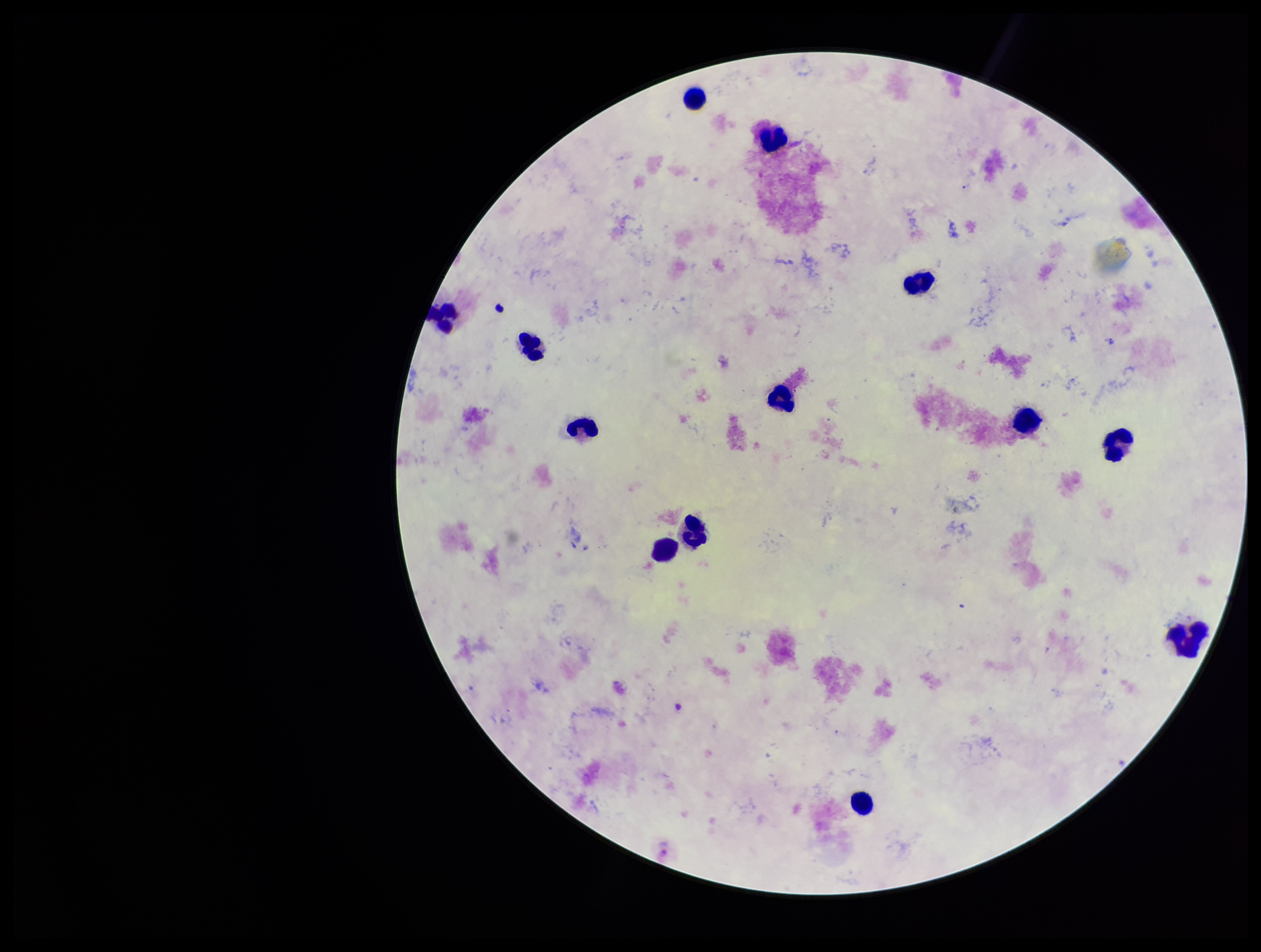 Preparation: thick blood smear. One field from this slide. Image is 1261×952 pixels. Species reported for this patient: Plasmodium vivax. Parasite count: 0. Leukocyte count: 13. Plasmodium parasites: none detected. Photographed through the microscope eyepiece with a smartphone camera. Patient malaria status: positive. Giemsa stain.